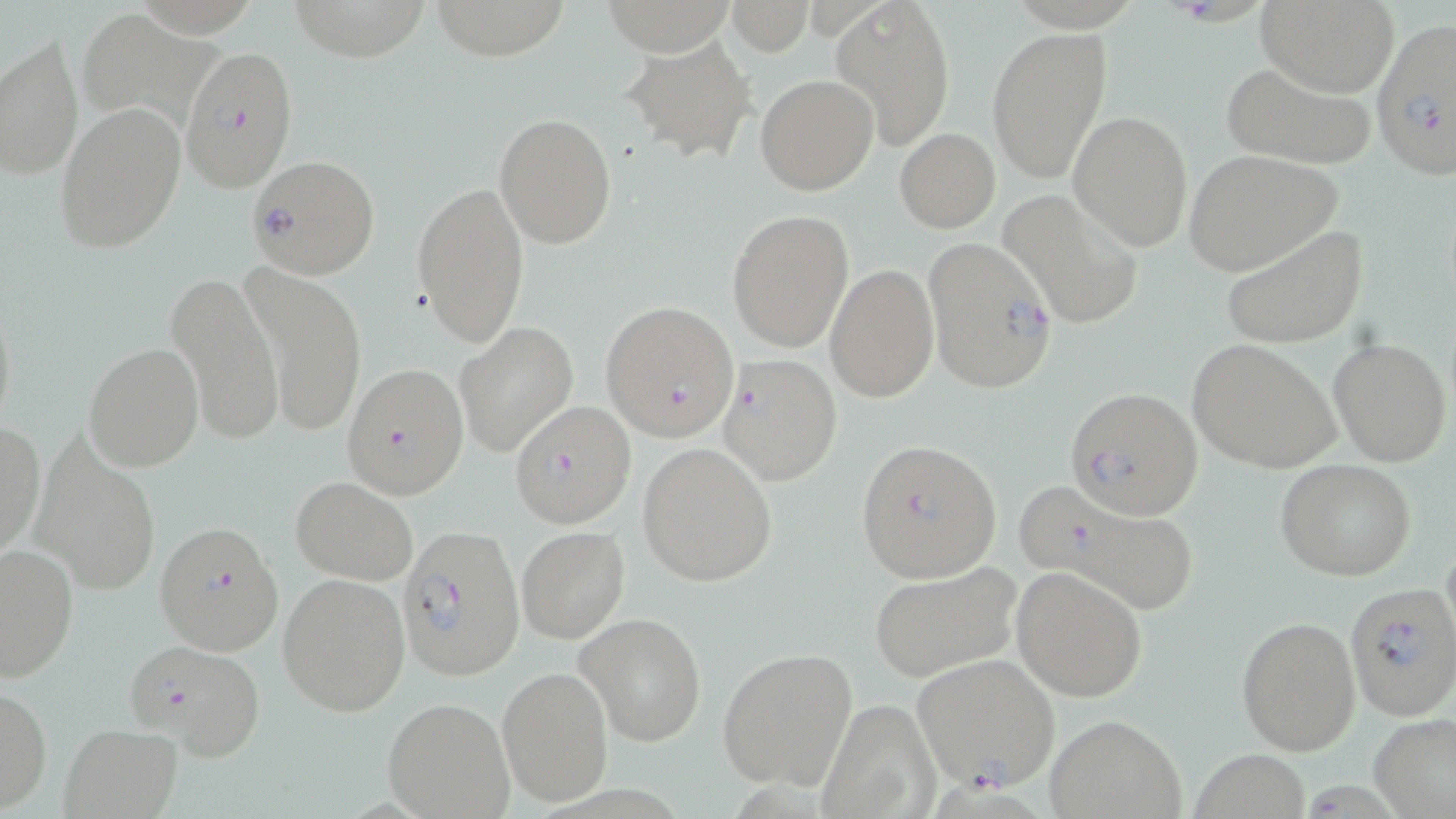
Approximate bounding boxes as (x1, y1, x2, y2) in pixels. Uninfected red blood cell locations: (135, 0, 265, 46), (291, 0, 426, 64), (435, 0, 563, 59), (831, 0, 956, 150), (1256, 0, 1399, 96), (725, 1, 814, 54), (82, 20, 227, 125), (986, 26, 1113, 187), (0, 32, 83, 180), (621, 33, 758, 163), (1219, 60, 1378, 170), (757, 74, 878, 195), (56, 101, 185, 254), (1070, 109, 1193, 254), (494, 112, 618, 247), (895, 129, 1000, 233), (1182, 150, 1342, 274), (411, 180, 529, 348), (1001, 188, 1144, 330), (727, 208, 854, 352), (1222, 224, 1367, 348), (825, 263, 939, 401), (240, 266, 367, 439), (166, 272, 284, 447), (1, 293, 17, 440), (456, 320, 578, 456), (1187, 337, 1344, 476), (1329, 338, 1451, 465), (82, 341, 202, 471), (1, 421, 45, 559), (34, 440, 162, 600), (637, 442, 778, 587), (1275, 458, 1416, 582), (290, 476, 418, 585), (516, 525, 629, 644), (0, 543, 77, 682), (868, 560, 1022, 682), (1012, 566, 1148, 702), (279, 573, 410, 716), (577, 612, 708, 746), (1237, 617, 1362, 756), (717, 647, 857, 790), (497, 665, 614, 806), (0, 685, 51, 812), (381, 696, 515, 819), (817, 697, 943, 818), (1370, 712, 1456, 818), (1045, 714, 1187, 818), (59, 724, 181, 818), (1191, 750, 1312, 819). Plasmodium falciparum-infected red blood cell locations: (1370, 14, 1456, 181), (181, 46, 294, 192), (246, 158, 380, 278), (921, 235, 1058, 395), (599, 301, 741, 442), (332, 354, 475, 501), (718, 355, 843, 486), (1065, 387, 1202, 519), (508, 401, 636, 528), (856, 438, 1002, 585), (1012, 477, 1205, 617), (155, 522, 284, 653), (396, 524, 523, 679), (1345, 585, 1455, 719), (123, 638, 267, 761), (912, 654, 1060, 791). Slide-level diagnosis: Plasmodium falciparum. Captured at 1000x magnification. Thin blood film. Image is 1456×819 pixels. Light microscopy. May-Grünwald-Giemsa-stained preparation. One field of a larger specimen.